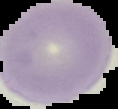

preparation = thin blood smear
image size = 118×109 pixels
malaria status = uninfected
image type = segmented cell region with the area outside set to black